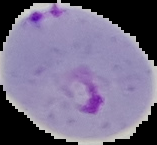
Summary:
  - Image type: segmented cell region on a black background
  - Preparation: thin blood smear
  - Image size: 157×145 pixels
  - Result: Plasmodium parasites detected